Identify the parasite.
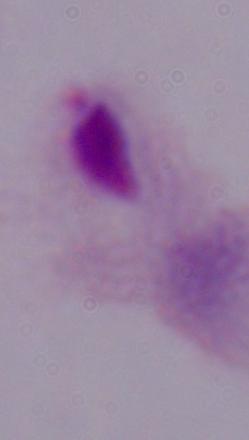

This is a trichomonad.

Photomicrograph. 1000x magnification.